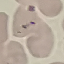
result: negative for malaria parasites
capture: smartphone through the microscope eyepiece
image_type: cell patch, automatically extracted from a larger field of view and resized to 64 × 64 pixels
stain: Giemsa
preparation: thin smear